Locate every Plasmodium parasite.
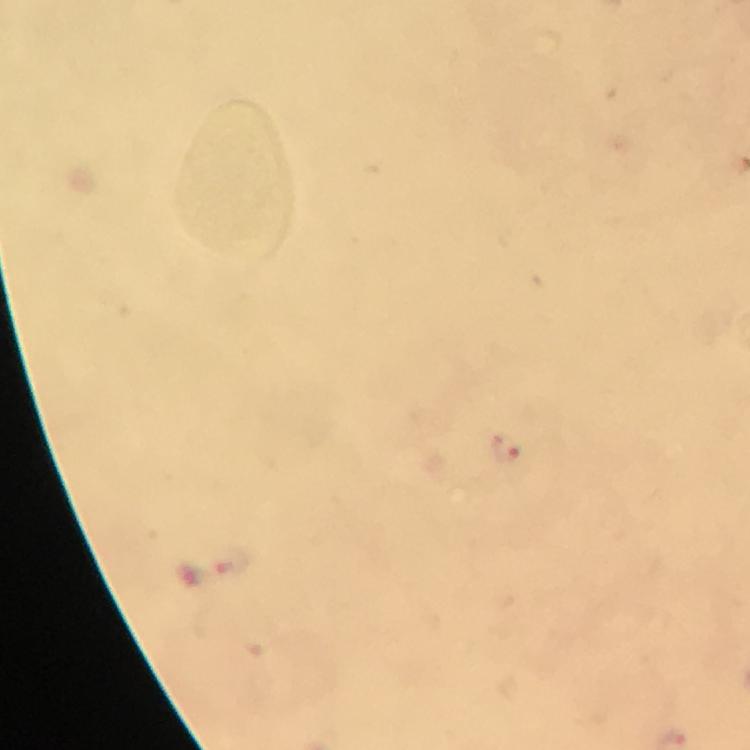

Approximate centers as (x, y) in pixels.
Plasmodium parasites: (506, 448).

Summary:
  - Capture: smartphone camera through the microscope
  - Image size: 750×750 pixels
  - Context: from a diagnostic examination for malaria
  - Preparation: thick smear
  - Immersion oil: used
  - Cropped from: a single field of view
  - Magnification: 100x
  - Stain: Giemsa